Give the preparation type.
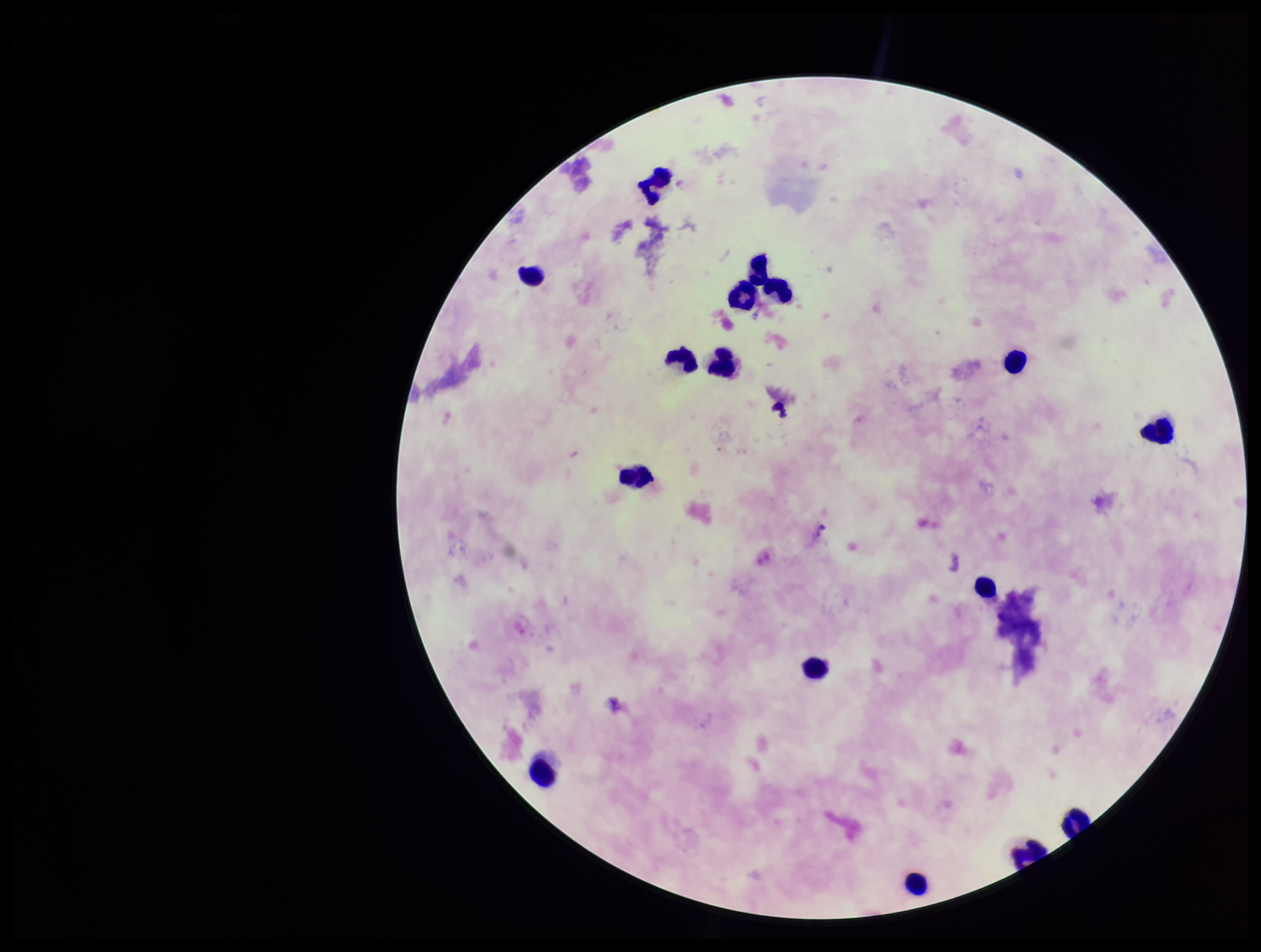
Thick.

{
  "patient_malaria_status": "infected",
  "species_reported_for_this_patient": "Plasmodium vivax",
  "plasmodium_parasites": "none identified",
  "leukocyte_count": 16,
  "stain": "Giemsa",
  "image_size": "1261×952 pixels",
  "parasite_count": 0,
  "field_of_view": "single",
  "capture": "smartphone photograph through the microscope eyepiece"
}